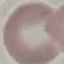
Summary:
  - Malaria status: uninfected
  - Preparation: thin smear
  - Image type: cell patch, automatically extracted from a larger field of view and resized to 64 × 64 pixels
  - Stain: Giemsa
  - Capture: smartphone through the microscope eyepiece